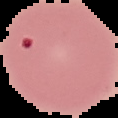

Summary:
  - Image type: segmented cell region with the area outside set to black
  - Preparation: thin blood smear
  - Result: malaria parasites detected
  - Image size: 118×118 pixels